Give the position of every Plasmodium parasite.
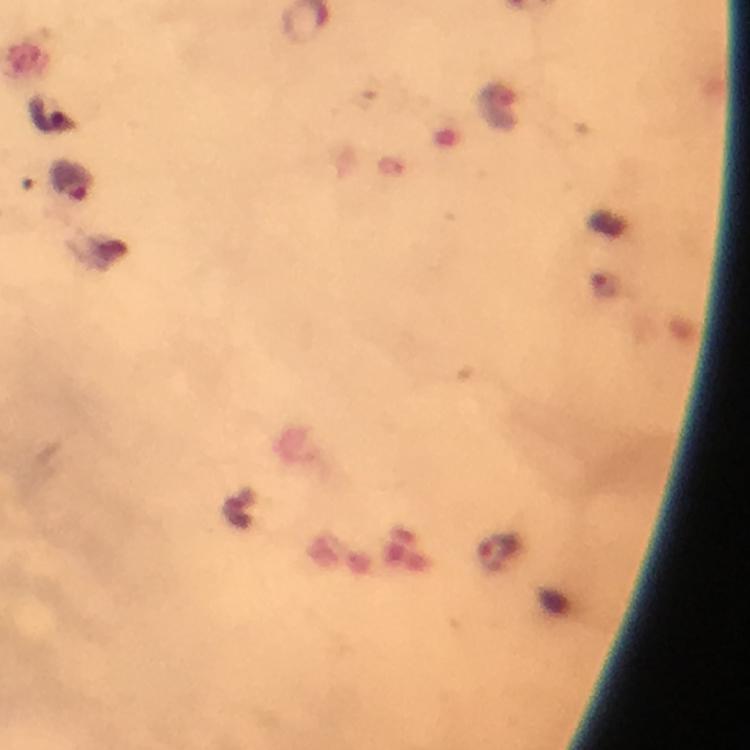

Approximate centers as (x, y) in pixels.
Plasmodium parasites: (45, 113), (70, 182), (497, 551).

Summary:
  - Capture: smartphone mounted on the microscope
  - Context: from a diagnostic examination for malaria
  - Stain: Giemsa
  - Immersion oil: used
  - Magnification: 100x
  - Cropped from: a single field of view
  - Image size: 750×750 pixels
  - Preparation: thick blood smear